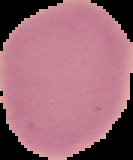

result = negative for Plasmodium parasites
image type = cell region segmented out of the field of view; surrounding area masked to black
preparation = thin blood film
image size = 133×160 pixels